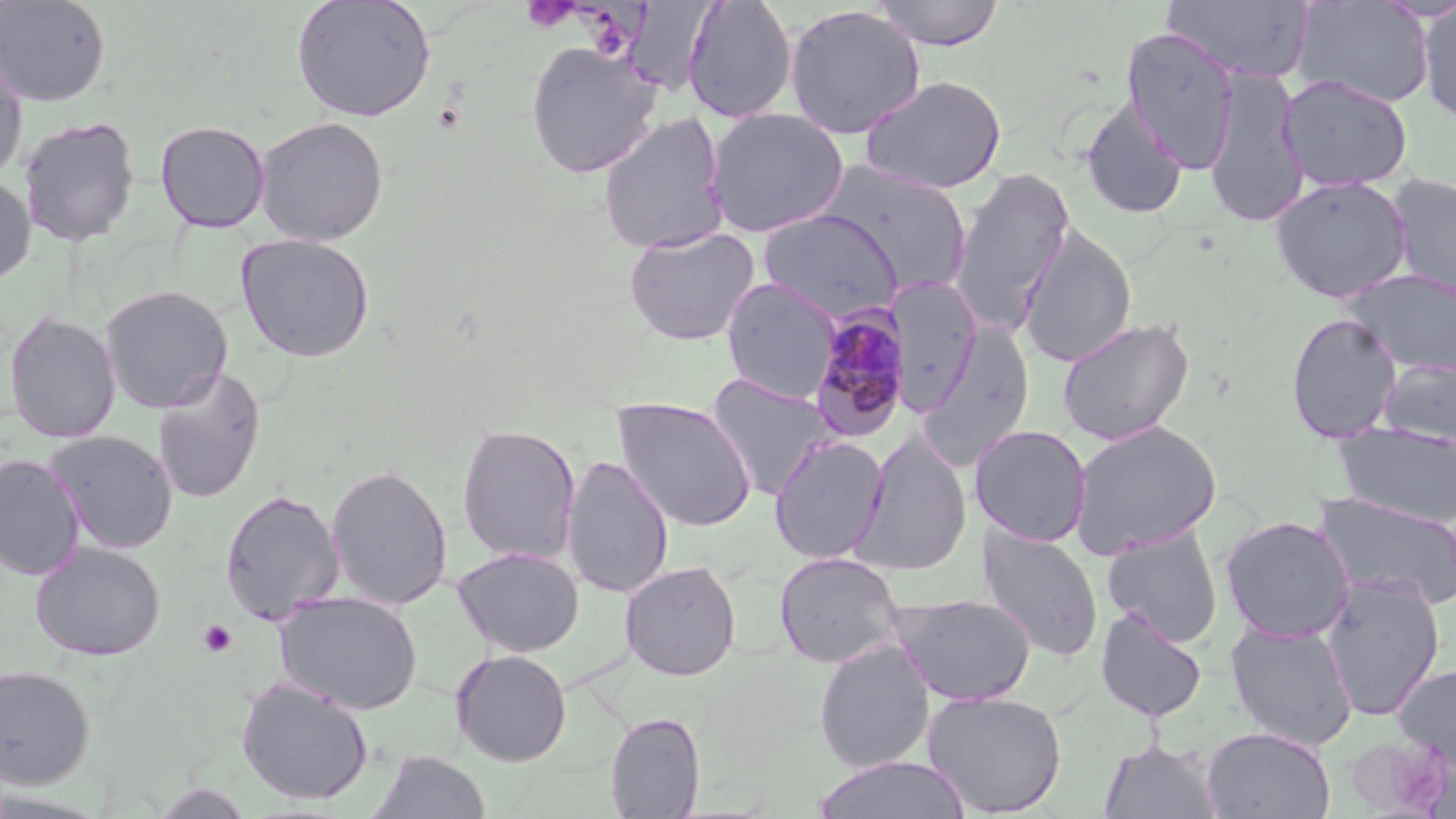
Approximate bounding boxes as (x1, y1, x2, y2) in pixels. Uninfected red blood cell locations: (0, 0, 112, 107), (291, 0, 436, 123), (682, 0, 798, 124), (870, 0, 1006, 50), (1161, 0, 1315, 83), (1293, 1, 1434, 109), (1417, 3, 1456, 124), (783, 4, 926, 140), (1121, 26, 1240, 173), (525, 40, 663, 178), (0, 51, 28, 186), (1203, 68, 1310, 227), (861, 74, 1007, 195), (1278, 74, 1413, 192), (1078, 97, 1189, 220), (705, 107, 850, 238), (597, 110, 731, 255), (19, 115, 140, 247), (255, 115, 389, 246), (155, 120, 271, 233), (815, 160, 972, 294), (947, 167, 1076, 337), (0, 173, 36, 285), (1386, 173, 1456, 303), (1270, 175, 1413, 304), (758, 209, 904, 322), (1015, 225, 1138, 368), (623, 226, 761, 346), (236, 232, 375, 363), (1343, 268, 1456, 379), (886, 276, 984, 413), (721, 277, 842, 404), (99, 285, 233, 413), (3, 310, 121, 444), (1285, 312, 1403, 444), (1056, 316, 1195, 445), (917, 324, 1036, 469), (1377, 358, 1456, 449), (151, 365, 266, 504), (705, 372, 838, 500), (613, 396, 757, 532), (1069, 419, 1222, 558), (1334, 421, 1456, 527), (456, 423, 582, 566), (969, 424, 1093, 547), (851, 428, 973, 577), (44, 430, 179, 555), (769, 434, 888, 564), (0, 453, 86, 581), (561, 453, 674, 598), (326, 463, 452, 610), (220, 489, 345, 624), (1315, 493, 1456, 611), (1220, 515, 1355, 643), (977, 524, 1104, 661), (1102, 527, 1223, 647), (30, 541, 165, 661), (452, 546, 585, 657), (773, 551, 906, 669), (620, 560, 742, 682), (1321, 576, 1446, 720), (274, 590, 422, 715), (889, 592, 1036, 705), (1095, 606, 1208, 723), (1225, 620, 1358, 749), (813, 640, 935, 773), (450, 648, 573, 766), (1392, 662, 1456, 771), (0, 663, 96, 788), (236, 677, 373, 805), (923, 689, 1068, 816), (604, 711, 705, 819), (1202, 726, 1335, 819), (1344, 734, 1453, 817), (1098, 739, 1222, 818), (367, 750, 491, 819), (811, 756, 972, 818), (148, 783, 256, 818). Plasmodium malariae-infected red blood cell locations: (807, 304, 912, 443). Platelet locations: (521, 2, 580, 33), (433, 102, 467, 135), (198, 620, 237, 657). Slide-level diagnosis: Plasmodium malariae. Thin blood film. Optical microscopy. May-Grünwald-Giemsa stain. Single field of view. 1000x magnification. Image is 1456×819 pixels.